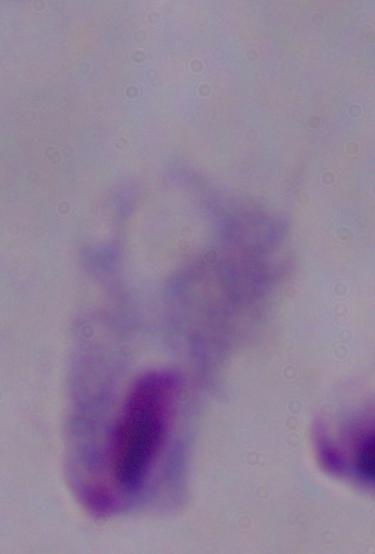

Summary:
  - Magnification: 1000x
  - Modality: micrograph
  - Identification: trichomonad